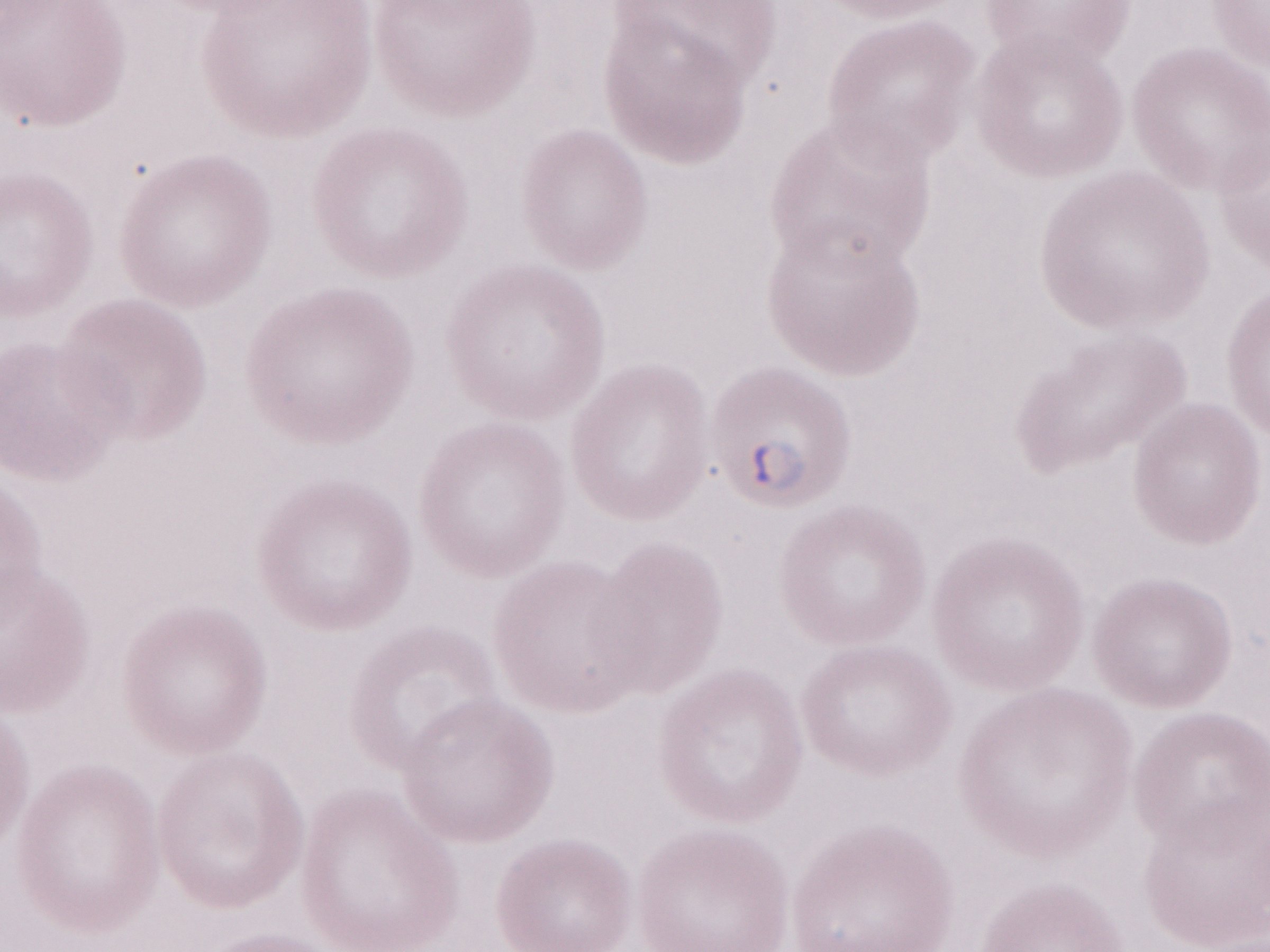

Image is 1270×952 pixels. 1,000x magnification. Olympus BX43 microscope, Olympus DP73 camera. May-Grünwald-Giemsa (MGG) stain. Thin blood film. Patient-level malaria diagnosis: positive. One field of this slide.